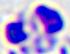

400x magnification. A leukocyte is seen. Photomicrograph.